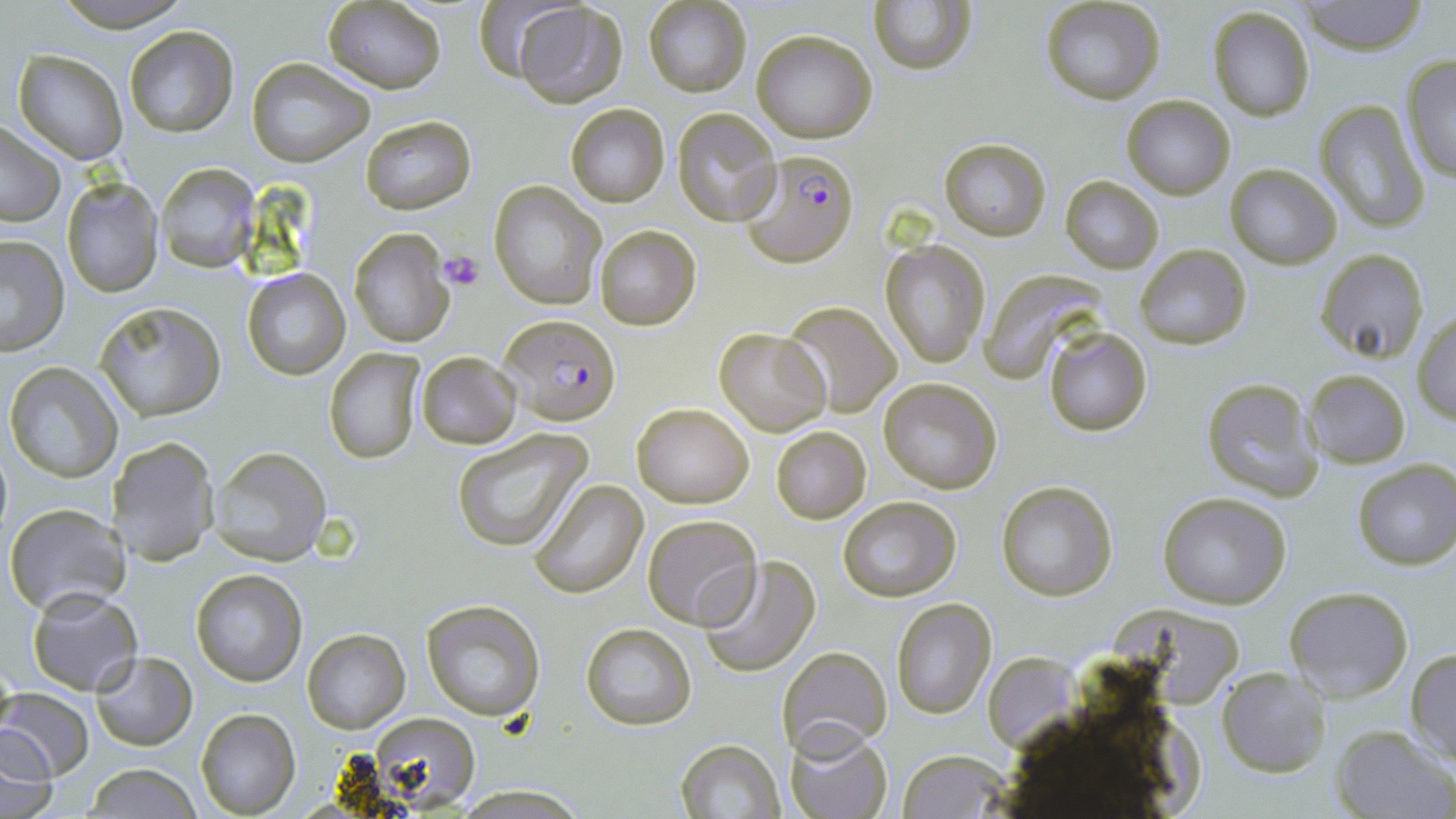
Summary:
  - Coordinate format: approximate bounding boxes as (x1,y1)-(x2,y2) corner pairs in pixels
  - Uninfected red blood cell locations: (46,0)-(197,29), (472,0)-(581,82), (1041,0)-(1164,106), (1299,0)-(1430,55), (644,1)-(750,97), (868,1)-(975,76), (320,2)-(446,91), (509,2)-(629,107), (1207,7)-(1317,121), (124,25)-(240,137), (751,29)-(877,143), (12,49)-(128,163), (1399,54)-(1456,182), (247,57)-(375,169), (1122,95)-(1233,199), (1315,100)-(1429,233), (566,104)-(669,206), (673,108)-(781,226), (361,114)-(476,215), (1,120)-(64,226), (939,138)-(1050,240), (154,162)-(262,273), (1226,164)-(1340,268), (61,175)-(164,297), (1061,177)-(1163,273), (488,181)-(605,310), (594,224)-(701,330), (349,228)-(457,348), (0,234)-(70,354), (882,240)-(990,368), (1135,245)-(1250,349), (1316,249)-(1431,365), (980,267)-(1106,381), (242,269)-(349,380), (97,301)-(225,421), (782,301)-(901,415), (1411,313)-(1456,424), (714,327)-(832,437), (1043,327)-(1153,439), (325,348)-(423,463), (416,352)-(520,448), (3,362)-(124,483), (1303,368)-(1412,468), (878,376)-(1002,493), (1200,377)-(1323,501), (632,401)-(754,508), (772,426)-(872,524), (453,429)-(592,552), (110,439)-(217,545), (206,446)-(335,550), (1352,460)-(1456,570), (528,478)-(649,599), (996,481)-(1117,601), (1157,492)-(1292,608), (837,496)-(960,601), (3,504)-(130,617), (641,515)-(761,628), (697,557)-(819,678), (189,568)-(307,687), (1284,586)-(1414,702), (25,588)-(142,695), (890,597)-(996,718), (420,599)-(543,719), (581,622)-(697,731), (301,628)-(410,732), (779,644)-(892,755), (1406,648)-(1456,767), (89,649)-(197,749), (1217,667)-(1330,778), (1,690)-(94,781), (194,708)-(301,817), (363,712)-(483,810), (1331,724)-(1455,818), (785,725)-(893,818), (0,730)-(59,817), (675,739)-(786,819), (895,750)-(1013,818), (83,765)-(201,818)
  - Platelet locations: (438,252)-(485,292)
  - Plasmodium falciparum-infected red blood cell locations: (739,147)-(862,265), (498,313)-(623,425)
  - Slide-level diagnosis: Plasmodium falciparum
  - Magnification: 1000x
  - Image size: 1456×819 pixels
  - Stain: May-Grünwald-Giemsa
  - Modality: light microscopy
  - Field of view: one of a larger specimen
  - Preparation: thin blood smear